Give the extent of all Babesia divergens-infected red blood cells.
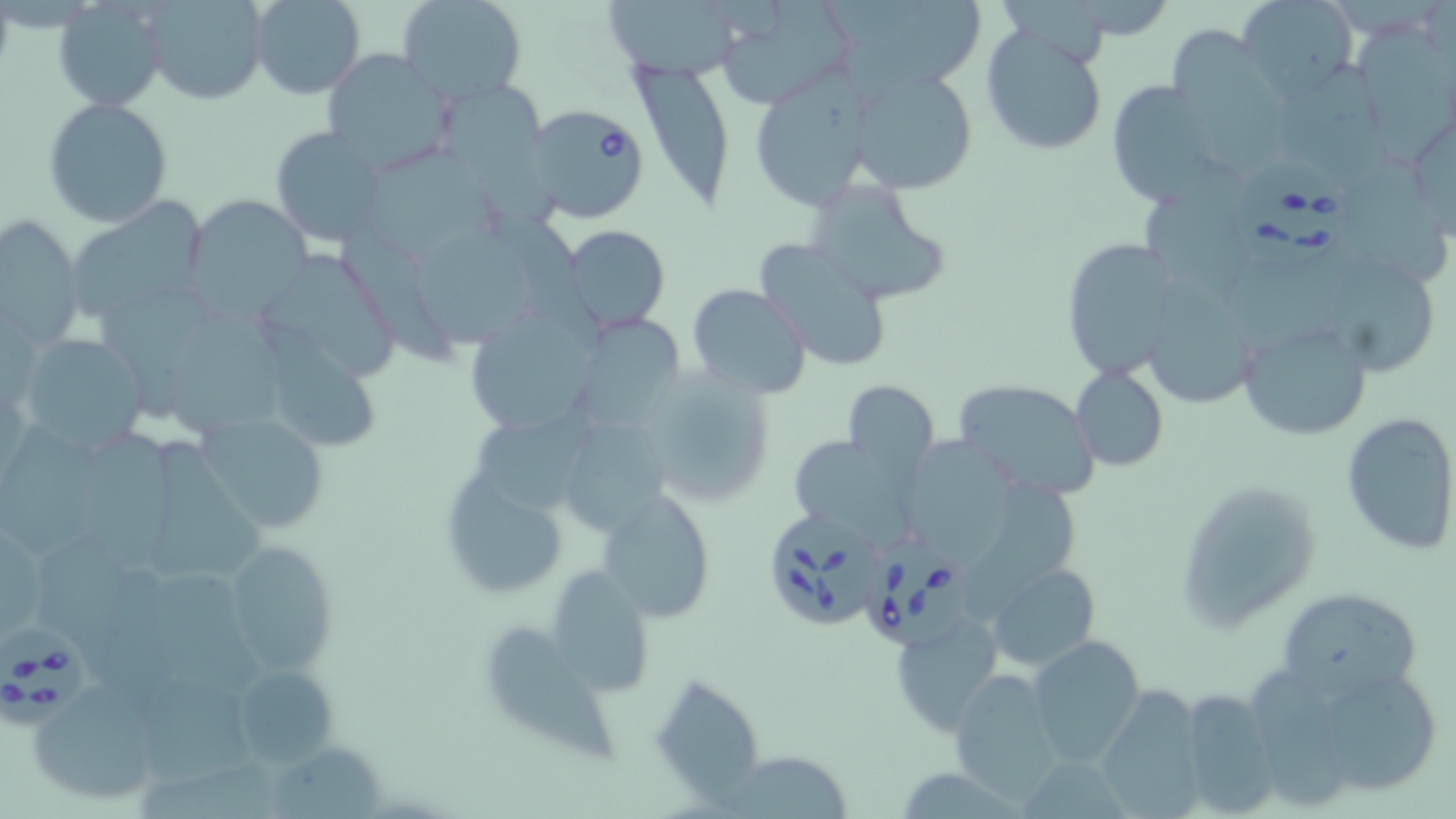
Approximate bounding boxes as named x1/y1/x2/y2 corners in pixels.
Babesia divergens-infected red blood cells: (x1=527, y1=104, x2=651, y2=225), (x1=1236, y1=159, x2=1353, y2=271), (x1=771, y1=513, x2=883, y2=627), (x1=865, y1=535, x2=983, y2=649), (x1=1, y1=623, x2=97, y2=724).

slide_level_diagnosis: Babesia divergens
stain: May-Grünwald-Giemsa
uninfected_red_blood_cell_locations: 'approximate bounding boxes as named x1/y1/x2/y2 corners in pixels: (x1=251, y1=0, x2=365, y2=99), (x1=397, y1=0, x2=527, y2=103), (x1=714, y1=0, x2=855, y2=110), (x1=846, y1=0, x2=987, y2=86), (x1=1237, y1=0, x2=1359, y2=98), (x1=142, y1=1, x2=268, y2=104), (x1=603, y1=1, x2=742, y2=79), (x1=52, y1=3, x2=168, y2=111), (x1=980, y1=24, x2=1110, y2=160), (x1=1358, y1=24, x2=1453, y2=161), (x1=1171, y1=39, x2=1308, y2=177), (x1=1284, y1=50, x2=1391, y2=192), (x1=321, y1=51, x2=457, y2=173), (x1=630, y1=61, x2=735, y2=209), (x1=846, y1=64, x2=979, y2=197), (x1=750, y1=76, x2=876, y2=210), (x1=1103, y1=79, x2=1230, y2=208), (x1=443, y1=82, x2=560, y2=231), (x1=42, y1=98, x2=173, y2=228), (x1=269, y1=125, x2=391, y2=249), (x1=370, y1=153, x2=500, y2=262), (x1=804, y1=178, x2=953, y2=305), (x1=1140, y1=185, x2=1249, y2=300), (x1=184, y1=196, x2=312, y2=317), (x1=65, y1=198, x2=210, y2=326), (x1=0, y1=217, x2=84, y2=351), (x1=558, y1=225, x2=671, y2=331), (x1=418, y1=226, x2=534, y2=354), (x1=335, y1=227, x2=454, y2=366), (x1=1059, y1=237, x2=1181, y2=376), (x1=756, y1=239, x2=895, y2=374), (x1=272, y1=257, x2=395, y2=379), (x1=1335, y1=260, x2=1438, y2=376), (x1=687, y1=283, x2=812, y2=401), (x1=1150, y1=284, x2=1263, y2=411), (x1=105, y1=290, x2=213, y2=419), (x1=472, y1=302, x2=602, y2=431), (x1=578, y1=314, x2=687, y2=435), (x1=1238, y1=318, x2=1372, y2=442), (x1=174, y1=319, x2=293, y2=444), (x1=260, y1=322, x2=379, y2=449), (x1=12, y1=334, x2=150, y2=455), (x1=1071, y1=366, x2=1169, y2=472), (x1=637, y1=368, x2=777, y2=506), (x1=842, y1=379, x2=940, y2=476), (x1=951, y1=379, x2=1101, y2=499), (x1=474, y1=402, x2=598, y2=521), (x1=1340, y1=411, x2=1456, y2=555), (x1=196, y1=413, x2=331, y2=535), (x1=1, y1=422, x2=109, y2=571), (x1=564, y1=422, x2=665, y2=541), (x1=81, y1=430, x2=186, y2=587), (x1=791, y1=435, x2=913, y2=540), (x1=904, y1=436, x2=1011, y2=567), (x1=151, y1=437, x2=266, y2=581), (x1=439, y1=476, x2=570, y2=601), (x1=1178, y1=478, x2=1320, y2=628), (x1=597, y1=489, x2=718, y2=623), (x1=984, y1=489, x2=1083, y2=610), (x1=220, y1=539, x2=337, y2=678), (x1=35, y1=546, x2=153, y2=689), (x1=544, y1=562, x2=656, y2=698), (x1=986, y1=562, x2=1099, y2=671), (x1=145, y1=566, x2=266, y2=697), (x1=1276, y1=585, x2=1428, y2=704), (x1=889, y1=611, x2=1001, y2=736), (x1=489, y1=624, x2=619, y2=761), (x1=1027, y1=635, x2=1145, y2=764), (x1=1288, y1=660, x2=1453, y2=802), (x1=227, y1=665, x2=336, y2=767), (x1=947, y1=668, x2=1064, y2=803), (x1=651, y1=673, x2=767, y2=808), (x1=144, y1=674, x2=263, y2=791), (x1=27, y1=682, x2=166, y2=808), (x1=1097, y1=686, x2=1209, y2=819), (x1=1174, y1=687, x2=1278, y2=816), (x1=723, y1=752, x2=854, y2=818)'
modality: light microscopy
magnification: 1000x
field_of_view: single
preparation: thin blood film
image_size: 1456×819 pixels